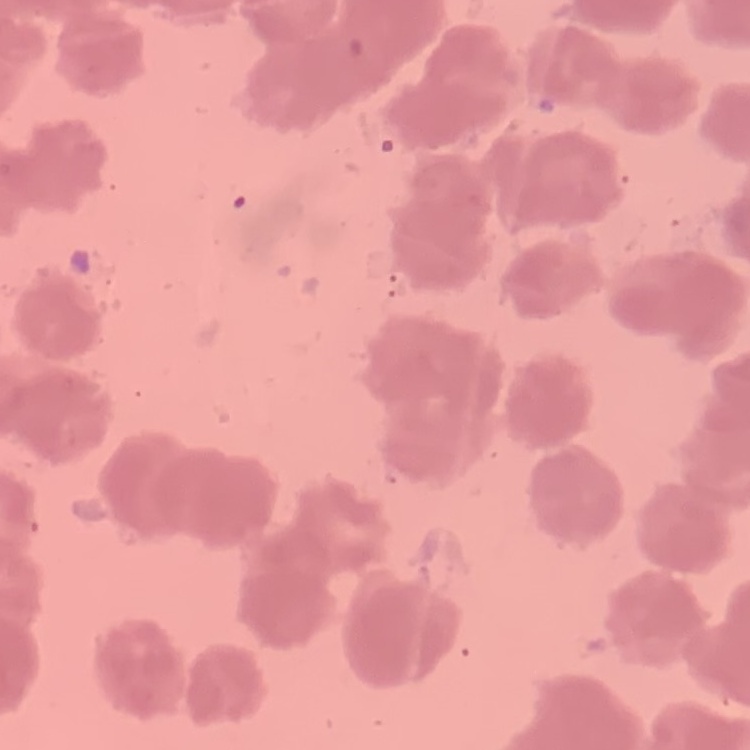

Summary:
  - Red blood cell morphology: rouleaux formation
  - Preparation: thin blood smear
  - Stain: Field's or Giemsa
  - Image type: square crop of a larger photomicrograph